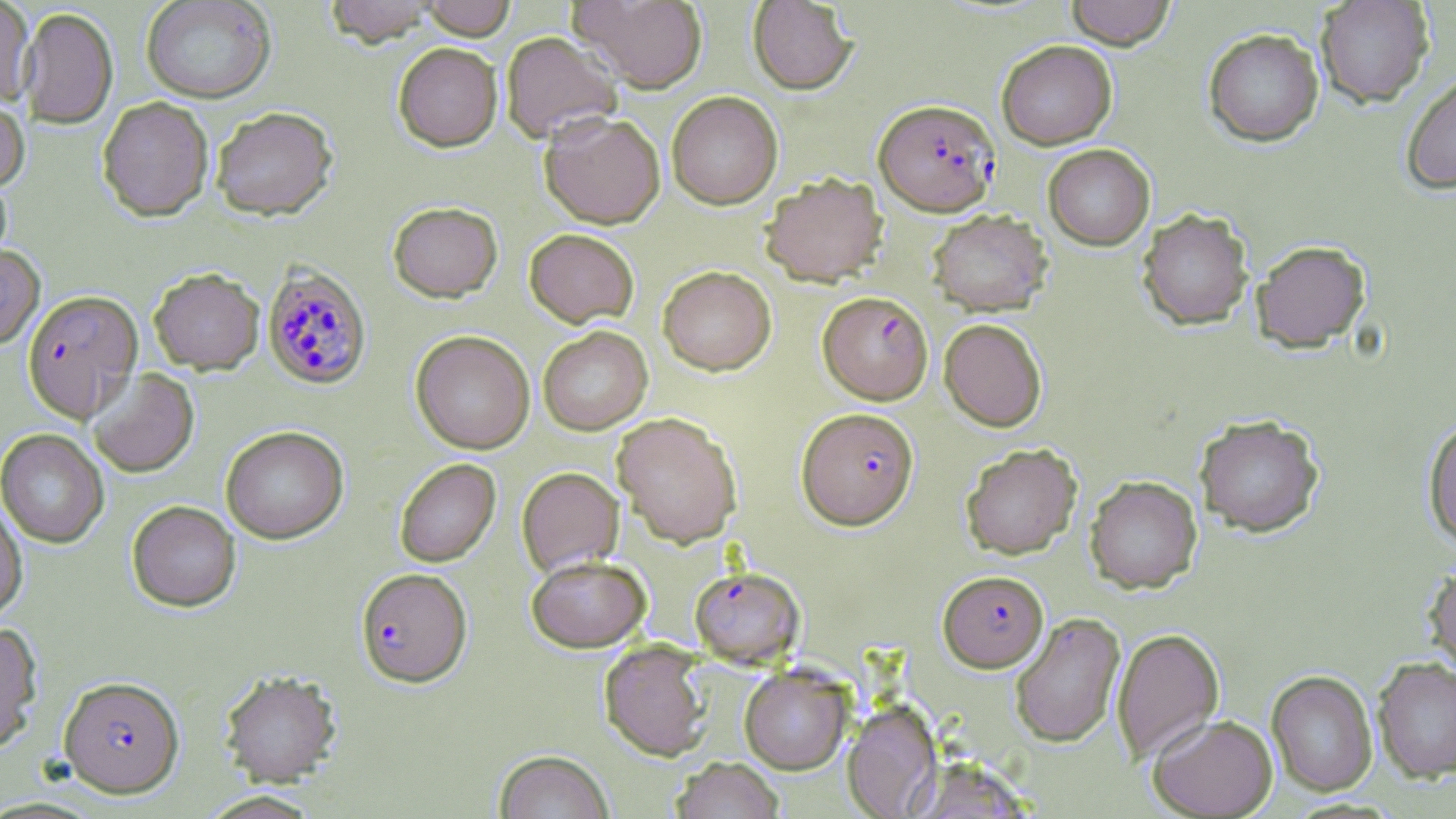

slide_level_diagnosis: Plasmodium falciparum
image_size: 1456×819 pixels
plasmodium_falciparum_infected_red_blood_cell_locations: 'approximate bounding boxes as named x1/y1/x2/y2 corners in pixels: (x1=874, y1=99, x2=1000, y2=216), (x1=262, y1=265, x2=372, y2=390), (x1=23, y1=291, x2=143, y2=423), (x1=818, y1=291, x2=932, y2=404), (x1=797, y1=407, x2=918, y2=529), (x1=689, y1=566, x2=805, y2=668), (x1=355, y1=567, x2=472, y2=687), (x1=938, y1=570, x2=1048, y2=672), (x1=58, y1=675, x2=185, y2=798)'
stain: May-Grünwald-Giemsa
uninfected_red_blood_cell_locations: 'approximate bounding boxes as named x1/y1/x2/y2 corners in pixels: (x1=0, y1=0, x2=35, y2=106), (x1=141, y1=0, x2=276, y2=104), (x1=324, y1=0, x2=438, y2=48), (x1=420, y1=0, x2=516, y2=40), (x1=569, y1=0, x2=708, y2=93), (x1=747, y1=0, x2=858, y2=94), (x1=1064, y1=0, x2=1177, y2=49), (x1=1315, y1=0, x2=1434, y2=108), (x1=19, y1=8, x2=118, y2=129), (x1=1203, y1=28, x2=1324, y2=147), (x1=500, y1=31, x2=622, y2=144), (x1=996, y1=40, x2=1117, y2=149), (x1=393, y1=43, x2=502, y2=153), (x1=1400, y1=71, x2=1456, y2=195), (x1=666, y1=91, x2=783, y2=209), (x1=0, y1=95, x2=29, y2=193), (x1=97, y1=97, x2=214, y2=223), (x1=211, y1=108, x2=338, y2=223), (x1=539, y1=110, x2=665, y2=229), (x1=1043, y1=144, x2=1155, y2=250), (x1=0, y1=168, x2=13, y2=275), (x1=761, y1=172, x2=888, y2=287), (x1=388, y1=201, x2=502, y2=303), (x1=1137, y1=208, x2=1254, y2=330), (x1=926, y1=209, x2=1053, y2=316), (x1=524, y1=228, x2=639, y2=327), (x1=1252, y1=239, x2=1370, y2=352), (x1=0, y1=244, x2=45, y2=350), (x1=658, y1=265, x2=776, y2=375), (x1=149, y1=268, x2=264, y2=375), (x1=939, y1=318, x2=1047, y2=431), (x1=538, y1=326, x2=652, y2=435), (x1=411, y1=331, x2=535, y2=454), (x1=87, y1=368, x2=200, y2=478), (x1=611, y1=412, x2=743, y2=548), (x1=1194, y1=414, x2=1325, y2=537), (x1=1422, y1=419, x2=1456, y2=550), (x1=221, y1=426, x2=349, y2=544), (x1=0, y1=429, x2=109, y2=549), (x1=960, y1=442, x2=1082, y2=559), (x1=394, y1=458, x2=501, y2=567), (x1=516, y1=467, x2=624, y2=577), (x1=1085, y1=475, x2=1202, y2=593), (x1=0, y1=498, x2=28, y2=622), (x1=127, y1=500, x2=241, y2=612), (x1=526, y1=554, x2=651, y2=652), (x1=1422, y1=562, x2=1456, y2=681), (x1=1009, y1=612, x2=1125, y2=748), (x1=0, y1=622, x2=44, y2=755), (x1=1111, y1=627, x2=1224, y2=764), (x1=599, y1=641, x2=712, y2=761), (x1=1372, y1=656, x2=1456, y2=783), (x1=739, y1=665, x2=852, y2=775), (x1=219, y1=669, x2=342, y2=787), (x1=1266, y1=669, x2=1378, y2=796), (x1=842, y1=700, x2=942, y2=818), (x1=1148, y1=713, x2=1278, y2=817), (x1=494, y1=750, x2=614, y2=819), (x1=671, y1=756, x2=784, y2=819), (x1=196, y1=790, x2=323, y2=818)'
magnification: 1000x
field_of_view: one of a larger specimen
preparation: thin blood smear
modality: light microscopy